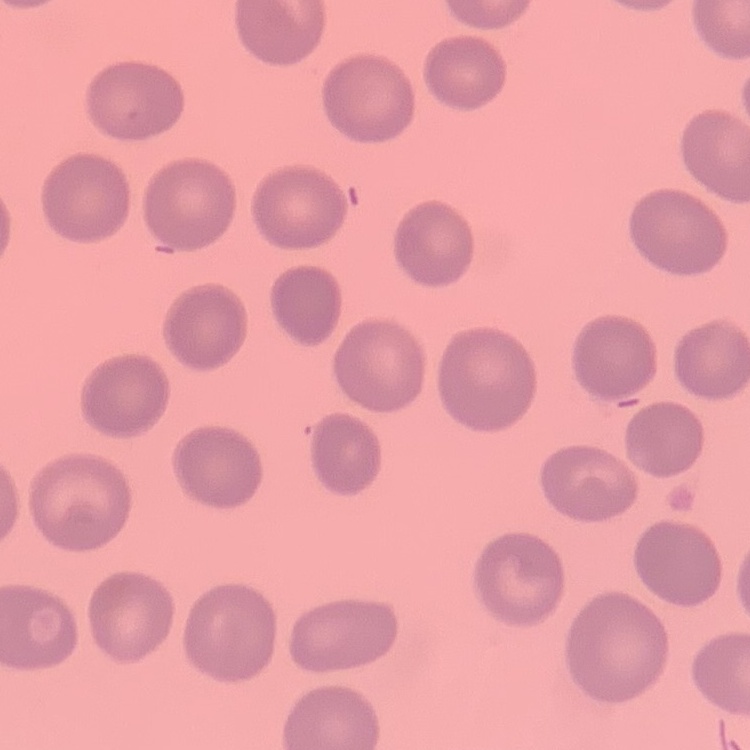
Summary:
  - Erythrocyte morphology: no rouleaux formation
  - Image type: one tile cut from a larger photomicrograph
  - Stain: Field's or Giemsa
  - Preparation: thin blood film